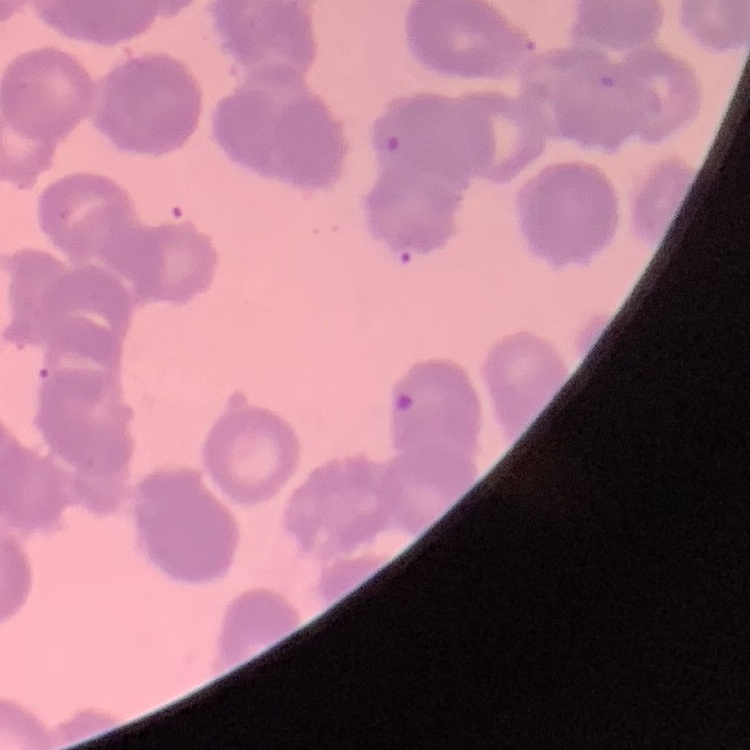
The erythrocytes exhibit rouleaux formation. One tile cut from a larger photomicrograph. Thin peripheral smear. Field's or Giemsa stain.